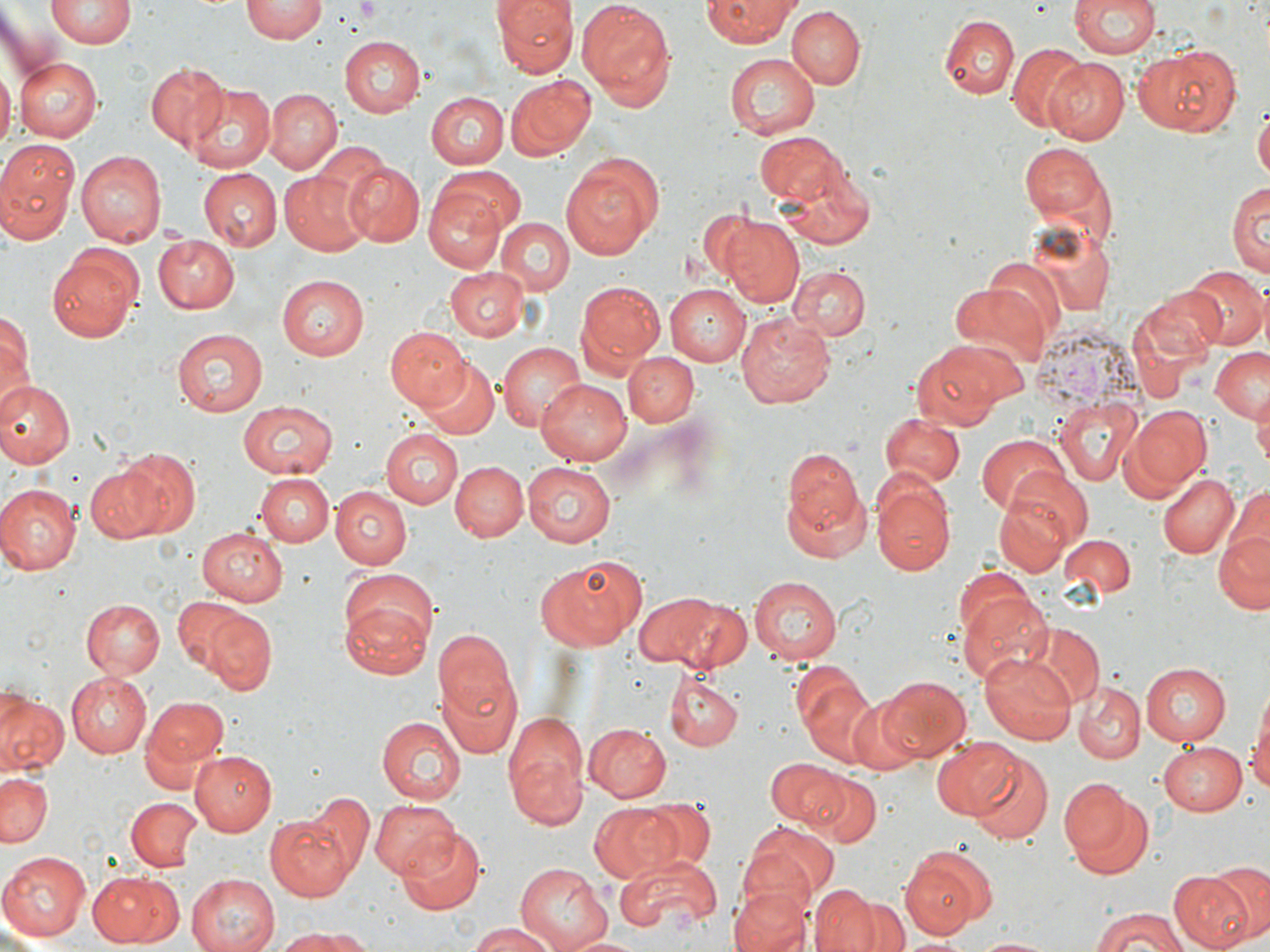
slide-level diagnosis = Plasmodium vivax
field of view = one of a larger specimen
image size = 1270×952 pixels
magnification = 1000x
modality = light microscopy
preparation = thin blood film
Plasmodium vivax-infected red blood cell locations = approximate bounding boxes as [x1, y1, x2, y2] in pixels: [1029, 321, 1151, 415]
uninfected red blood cell locations = approximate bounding boxes as [x1, y1, x2, y2] in pixels: [241, 0, 327, 43], [492, 0, 574, 76], [578, 0, 676, 102], [1069, 0, 1162, 58], [47, 1, 137, 47], [704, 1, 796, 45], [788, 6, 867, 88], [938, 13, 1019, 101], [339, 36, 425, 117], [1009, 44, 1090, 132], [1132, 44, 1241, 137], [724, 52, 821, 139], [13, 57, 102, 142], [1043, 57, 1130, 145], [145, 61, 231, 150], [0, 69, 15, 146], [505, 75, 594, 161], [185, 82, 274, 172], [265, 90, 340, 172], [425, 92, 509, 169], [1256, 101, 1270, 186], [758, 132, 845, 204], [0, 139, 81, 236], [1022, 143, 1109, 221], [77, 151, 165, 246], [561, 152, 665, 259], [779, 161, 876, 250], [343, 163, 424, 245], [435, 163, 525, 237], [200, 169, 280, 251], [279, 172, 368, 255], [1229, 179, 1269, 280], [424, 185, 508, 274], [722, 213, 805, 305], [495, 217, 572, 296], [153, 235, 239, 312], [48, 249, 143, 342], [983, 258, 1068, 340], [792, 265, 869, 342], [1184, 265, 1267, 351], [444, 267, 526, 342], [277, 274, 370, 359], [576, 280, 666, 375], [947, 282, 1048, 369], [664, 283, 750, 366], [1136, 286, 1226, 365], [0, 305, 33, 405], [738, 313, 834, 407], [171, 326, 271, 416], [386, 326, 471, 412], [909, 341, 1015, 428], [497, 343, 587, 433], [1210, 347, 1270, 426], [624, 351, 698, 427], [419, 360, 499, 439], [535, 378, 632, 466], [0, 379, 74, 466], [1056, 397, 1143, 487], [236, 399, 336, 478], [1255, 400, 1270, 473], [1125, 405, 1211, 496], [880, 413, 965, 487], [379, 429, 462, 506], [976, 434, 1069, 515], [780, 445, 870, 561], [105, 450, 198, 541], [449, 461, 526, 542], [520, 462, 617, 547], [998, 462, 1093, 549], [87, 465, 158, 541], [1157, 471, 1239, 559], [256, 473, 333, 548], [870, 474, 956, 577], [1222, 482, 1269, 590], [0, 485, 81, 575], [332, 487, 412, 569], [995, 490, 1079, 576], [1214, 524, 1270, 615], [197, 526, 290, 606], [1062, 535, 1137, 597], [533, 556, 645, 651], [748, 576, 844, 664], [956, 587, 1054, 686], [338, 588, 437, 677], [630, 589, 744, 671], [170, 594, 264, 684], [80, 598, 164, 679], [204, 612, 278, 697], [1025, 622, 1103, 706], [432, 627, 520, 754], [979, 653, 1075, 745], [1139, 662, 1231, 745], [66, 673, 151, 758], [663, 673, 742, 750], [878, 676, 973, 764], [801, 681, 888, 770], [1073, 682, 1145, 763], [0, 692, 68, 774], [843, 693, 926, 775], [143, 695, 228, 779], [1248, 697, 1270, 805], [502, 710, 592, 829], [376, 715, 464, 802], [584, 723, 671, 802], [932, 736, 1020, 818], [1157, 743, 1246, 817], [188, 750, 276, 836], [968, 751, 1053, 845], [766, 756, 849, 830], [802, 768, 880, 847], [0, 770, 52, 846], [1059, 777, 1138, 862], [308, 793, 371, 875], [369, 796, 458, 877], [127, 798, 200, 871], [643, 798, 715, 871], [587, 802, 678, 882], [265, 814, 353, 900], [740, 823, 836, 913], [394, 829, 488, 914], [902, 848, 994, 941], [0, 850, 92, 943], [614, 852, 721, 938], [512, 863, 613, 951], [1210, 863, 1270, 940], [1170, 871, 1255, 952], [90, 872, 181, 946], [185, 874, 279, 952], [812, 884, 881, 952], [729, 886, 813, 952], [851, 898, 909, 952], [1089, 909, 1191, 951], [464, 922, 559, 952], [278, 929, 371, 951], [566, 931, 643, 951], [972, 936, 1060, 952]
stain = May-Grünwald-Giemsa
platelet locations = approximate bounding boxes as [x1, y1, x2, y2] in pixels: [348, 0, 384, 24]